Name the blood parasite species.
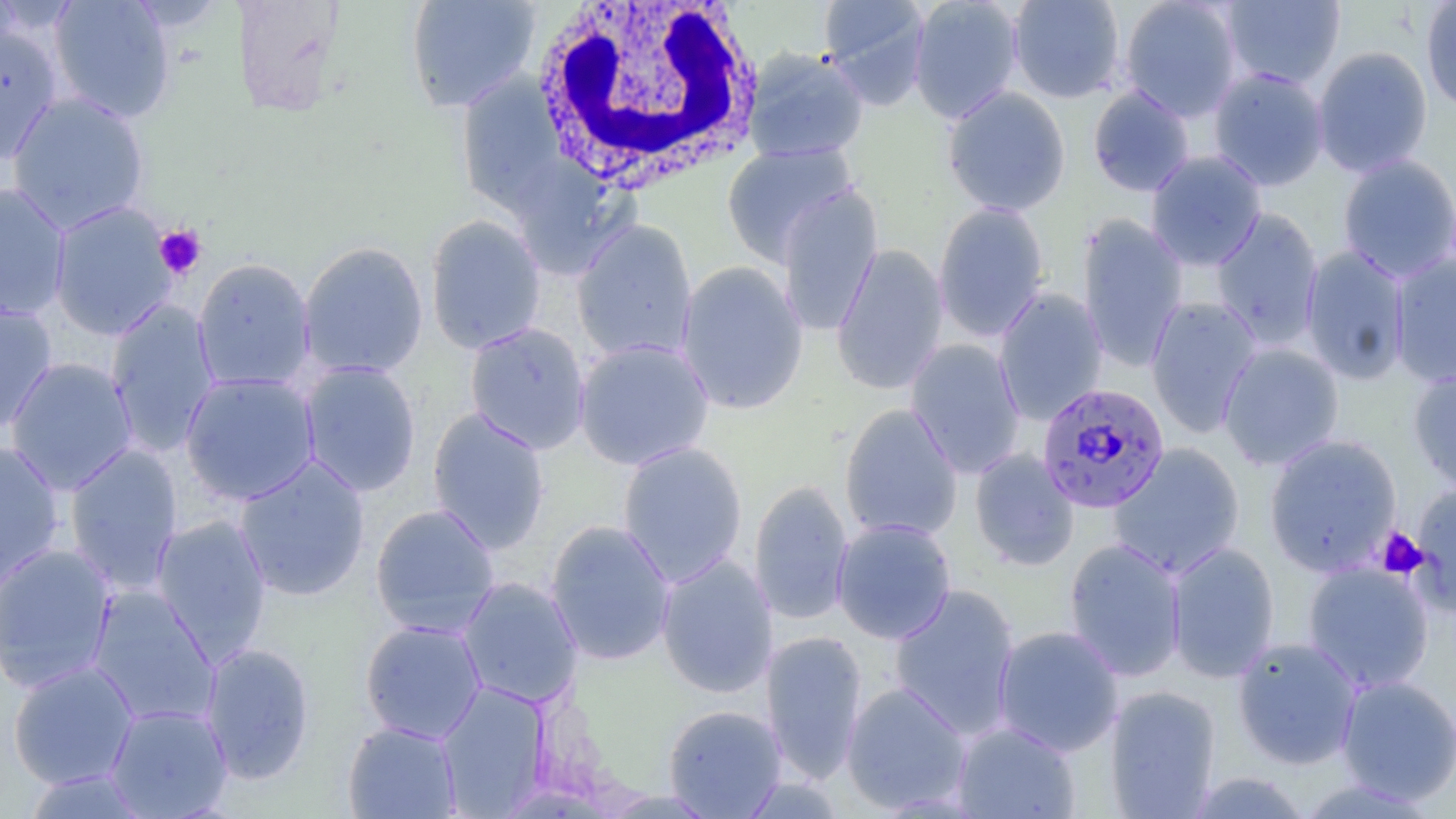
Plasmodium falciparum.

{
  "platelet_locations": "approximate bounding boxes as [x1, y1, x2, y2] in pixels: [154, 224, 207, 281], [1375, 527, 1429, 579]",
  "white_blood_cell_locations": "approximate bounding boxes as [x1, y1, x2, y2] in pixels: [529, 0, 765, 194]",
  "modality": "optical microscopy",
  "image_size": "1456×819 pixels",
  "field_of_view": "single",
  "plasmodium_falciparum_infected_red_blood_cell_locations": "approximate bounding boxes as [x1, y1, x2, y2] in pixels: [1036, 381, 1170, 514]",
  "stain": "May-Grünwald-Giemsa",
  "uninfected_red_blood_cell_locations": "approximate bounding boxes as [x1, y1, x2, y2] in pixels: [48, 0, 176, 123], [232, 0, 346, 117], [405, 0, 541, 113], [819, 0, 932, 107], [909, 0, 1024, 124], [1007, 0, 1125, 104], [1119, 0, 1242, 122], [1219, 1, 1345, 90], [1420, 1, 1456, 113], [0, 23, 63, 165], [1312, 46, 1433, 178], [743, 48, 868, 163], [1208, 67, 1329, 191], [456, 74, 567, 215], [1088, 85, 1195, 197], [942, 86, 1071, 217], [6, 91, 150, 233], [721, 143, 857, 265], [1145, 150, 1267, 271], [1337, 154, 1456, 283], [506, 157, 635, 280], [0, 181, 71, 321], [775, 182, 883, 337], [48, 201, 177, 340], [933, 201, 1049, 343], [1209, 207, 1324, 349], [425, 214, 546, 355], [1077, 214, 1188, 370], [572, 219, 698, 363], [297, 241, 429, 379], [831, 244, 949, 396], [1300, 245, 1411, 385], [1389, 254, 1456, 389], [192, 257, 316, 393], [676, 261, 809, 416], [994, 288, 1109, 425], [1145, 295, 1262, 438], [0, 299, 57, 434], [105, 300, 219, 456], [464, 322, 591, 454], [574, 338, 715, 471], [905, 339, 1026, 479], [1218, 342, 1344, 471], [3, 357, 138, 495], [299, 361, 422, 497], [1408, 365, 1456, 494], [180, 372, 321, 505], [839, 403, 963, 542], [427, 407, 550, 554], [1263, 434, 1402, 576], [0, 440, 65, 592], [617, 441, 748, 587], [1109, 443, 1245, 578], [63, 444, 184, 594], [969, 449, 1080, 571], [234, 455, 371, 602], [749, 480, 854, 626], [1410, 481, 1456, 612], [370, 503, 500, 638], [151, 514, 273, 664], [544, 519, 676, 666], [832, 519, 957, 644], [1063, 537, 1187, 682], [1166, 541, 1280, 684], [0, 542, 118, 693], [656, 554, 778, 699], [1301, 562, 1435, 694], [457, 576, 583, 709], [888, 584, 1021, 739], [87, 586, 220, 728], [359, 619, 486, 743], [992, 625, 1124, 756], [761, 630, 868, 784], [1232, 636, 1362, 770], [200, 642, 315, 784], [7, 660, 140, 790], [1336, 675, 1456, 805], [436, 681, 551, 816], [841, 681, 971, 814], [1105, 685, 1221, 818], [105, 703, 233, 818], [663, 704, 787, 818], [342, 720, 462, 818], [952, 721, 1081, 818], [21, 768, 152, 818], [1184, 771, 1314, 817], [1293, 778, 1441, 818]",
  "preparation": "thin blood film",
  "magnification": "1000x"
}